Locate and identify every blood parasite.
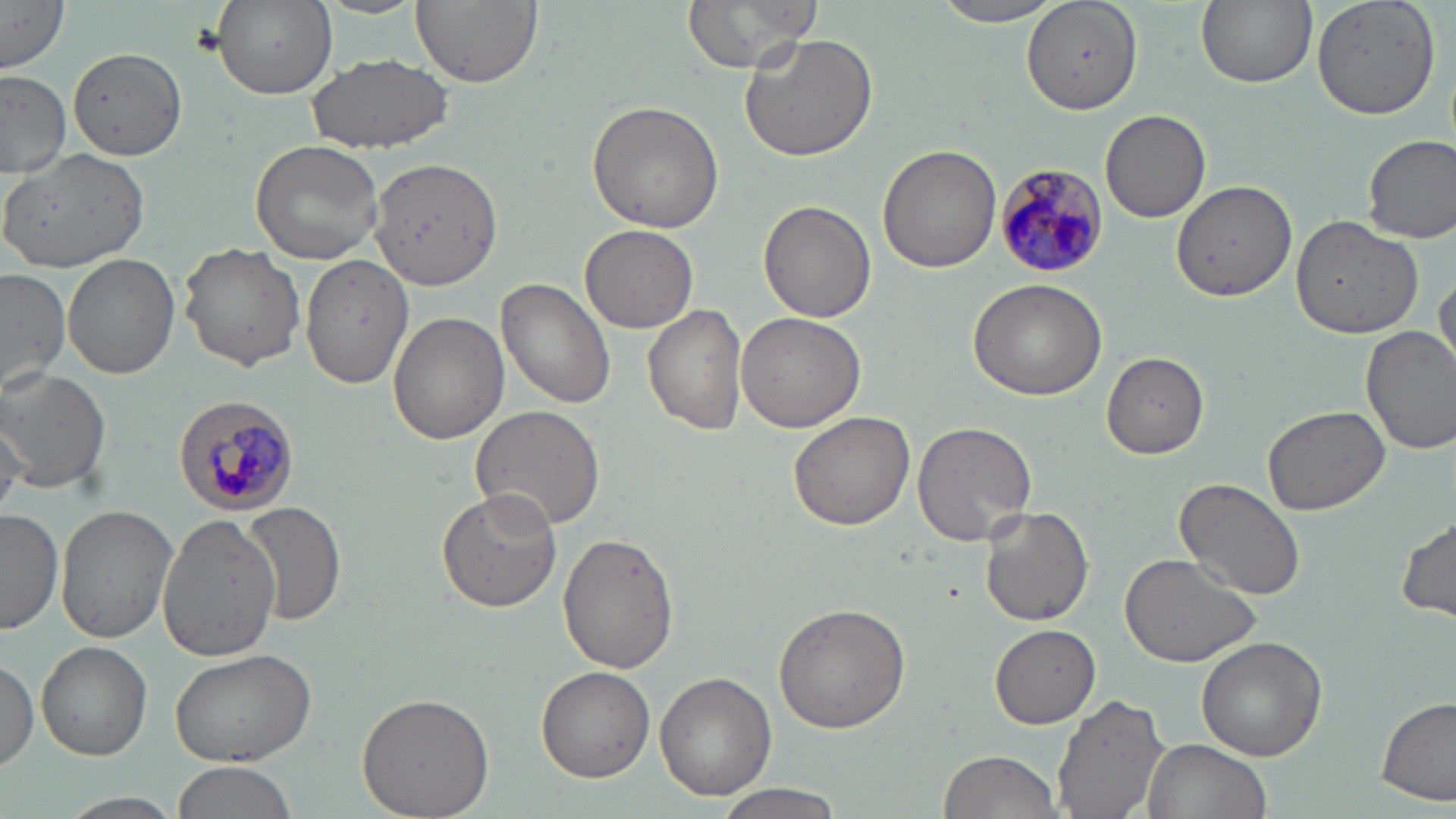
Approximate bounding boxes as named x1/y1/x2/y2 corners in pixels.
Plasmodium malariae-infected red blood cells: (x1=993, y1=162, x2=1111, y2=276), (x1=175, y1=395, x2=301, y2=516).
No Plasmodium falciparum, Plasmodium ovale, Plasmodium vivax, Babesia divergens, or Trypanosoma brucei observed.

slide-level diagnosis = Plasmodium malariae
uninfected red blood cell locations = approximate bounding boxes as named x1/y1/x2/y2 corners in pixels: (x1=1, y1=0, x2=69, y2=72), (x1=213, y1=0, x2=338, y2=99), (x1=410, y1=0, x2=542, y2=88), (x1=681, y1=0, x2=825, y2=73), (x1=935, y1=0, x2=1064, y2=27), (x1=1025, y1=0, x2=1143, y2=116), (x1=1195, y1=0, x2=1317, y2=89), (x1=1312, y1=0, x2=1442, y2=120), (x1=739, y1=29, x2=880, y2=161), (x1=69, y1=47, x2=185, y2=162), (x1=305, y1=52, x2=453, y2=155), (x1=1, y1=69, x2=69, y2=178), (x1=585, y1=100, x2=725, y2=234), (x1=1101, y1=110, x2=1210, y2=221), (x1=1362, y1=135, x2=1456, y2=244), (x1=250, y1=139, x2=384, y2=263), (x1=877, y1=142, x2=1002, y2=272), (x1=4, y1=146, x2=151, y2=275), (x1=364, y1=157, x2=502, y2=293), (x1=1171, y1=180, x2=1298, y2=303), (x1=757, y1=200, x2=877, y2=322), (x1=1291, y1=215, x2=1426, y2=338), (x1=580, y1=223, x2=698, y2=333), (x1=179, y1=242, x2=307, y2=371), (x1=62, y1=251, x2=181, y2=378), (x1=300, y1=253, x2=413, y2=389), (x1=0, y1=267, x2=71, y2=393), (x1=1432, y1=267, x2=1455, y2=377), (x1=496, y1=277, x2=617, y2=410), (x1=967, y1=277, x2=1108, y2=400), (x1=643, y1=304, x2=749, y2=436), (x1=388, y1=312, x2=508, y2=445), (x1=733, y1=312, x2=868, y2=433), (x1=1361, y1=325, x2=1456, y2=452), (x1=1101, y1=352, x2=1211, y2=459), (x1=0, y1=365, x2=113, y2=495), (x1=1263, y1=404, x2=1389, y2=515), (x1=470, y1=405, x2=606, y2=532), (x1=787, y1=410, x2=913, y2=532), (x1=0, y1=417, x2=29, y2=519), (x1=911, y1=419, x2=1038, y2=546), (x1=1174, y1=478, x2=1308, y2=602), (x1=436, y1=488, x2=563, y2=611), (x1=244, y1=501, x2=348, y2=628), (x1=56, y1=503, x2=178, y2=643), (x1=978, y1=505, x2=1093, y2=626), (x1=0, y1=508, x2=62, y2=634), (x1=157, y1=511, x2=281, y2=661), (x1=1396, y1=512, x2=1455, y2=623), (x1=558, y1=532, x2=678, y2=673), (x1=1119, y1=553, x2=1263, y2=669), (x1=774, y1=601, x2=913, y2=733), (x1=990, y1=624, x2=1101, y2=726), (x1=1197, y1=636, x2=1328, y2=761), (x1=39, y1=641, x2=152, y2=760), (x1=168, y1=646, x2=320, y2=766), (x1=0, y1=654, x2=39, y2=772), (x1=537, y1=666, x2=656, y2=781), (x1=656, y1=672, x2=777, y2=800), (x1=355, y1=692, x2=494, y2=818), (x1=1052, y1=692, x2=1172, y2=819), (x1=1377, y1=694, x2=1454, y2=806), (x1=1141, y1=739, x2=1271, y2=819), (x1=937, y1=749, x2=1064, y2=819), (x1=167, y1=761, x2=296, y2=819), (x1=711, y1=780, x2=851, y2=819)
modality = optical microscopy
image size = 1456×819 pixels
magnification = 1000x
stain = May-Grünwald-Giemsa
preparation = thin blood film
field of view = single